Report the malaria status of this cell.
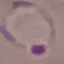
It is parasitized.

Thin blood smear. Cell patch, automatically extracted from a larger field of view and resized to 64 × 64 pixels. Giemsa-stained preparation. Acquired by smartphone through the microscope eyepiece.